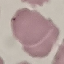

malaria_status: uninfected
capture: smartphone through the microscope eyepiece
stain: Giemsa
preparation: thin blood film
image_type: cell patch, automatically extracted from a larger field of view and resized to 64 × 64 pixels